Give the extent of all Plasmodium ovale-infected red blood cells.
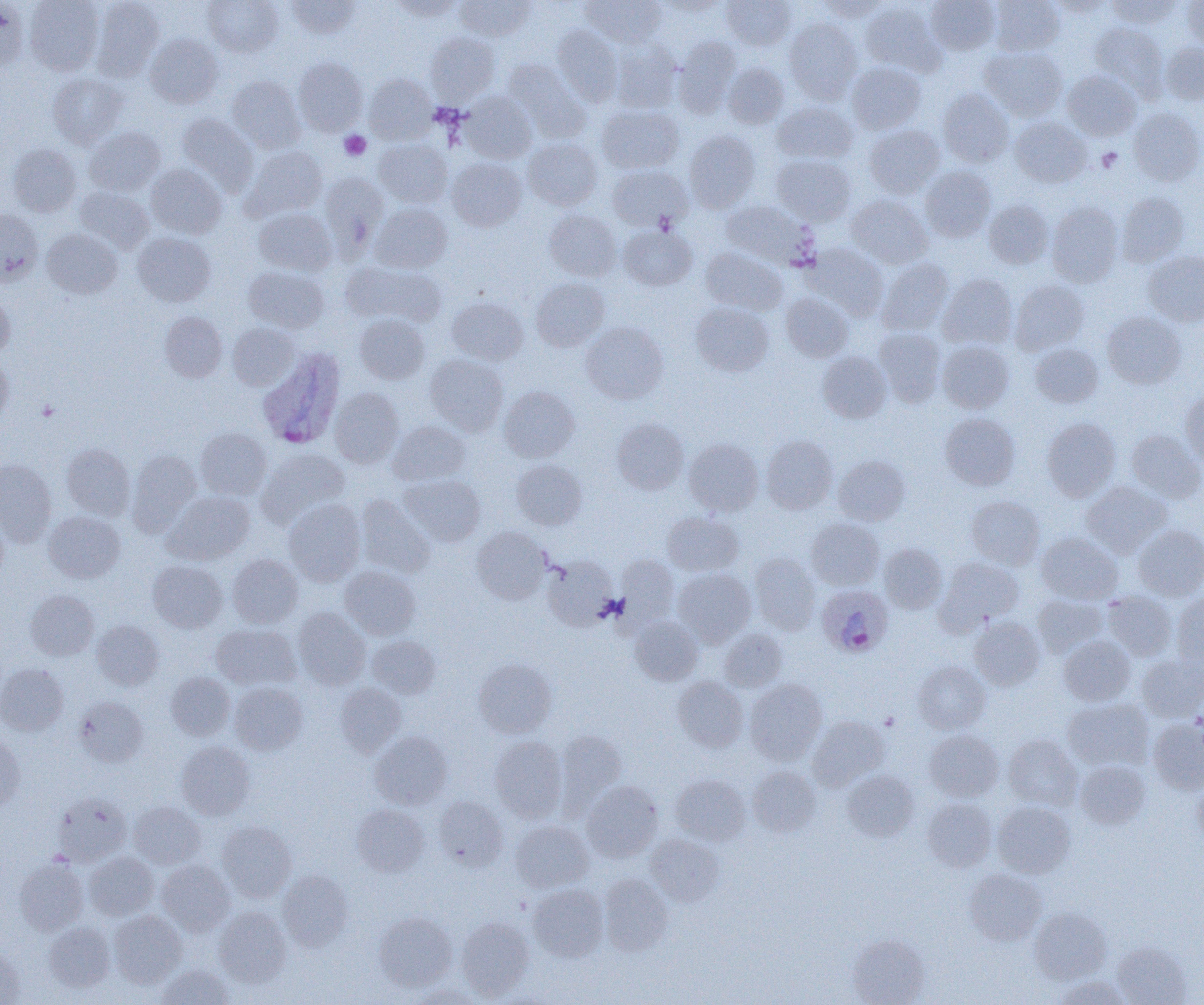

Approximate bounding boxes as named x1/y1/x2/y2 corners in pixels.
Plasmodium ovale-infected red blood cells: (x1=257, y1=348, x2=345, y2=449), (x1=816, y1=584, x2=893, y2=658).

Platelet locations: (x1=339, y1=131, x2=371, y2=160), (x1=1097, y1=148, x2=1122, y2=172), (x1=37, y1=400, x2=59, y2=421). Uninfected red blood cell locations: (x1=0, y1=0, x2=29, y2=74), (x1=24, y1=0, x2=104, y2=75), (x1=91, y1=0, x2=165, y2=81), (x1=203, y1=0, x2=283, y2=57), (x1=287, y1=0, x2=360, y2=39), (x1=389, y1=0, x2=464, y2=21), (x1=455, y1=0, x2=534, y2=41), (x1=582, y1=0, x2=665, y2=48), (x1=721, y1=0, x2=796, y2=50), (x1=813, y1=0, x2=890, y2=22), (x1=926, y1=0, x2=999, y2=55), (x1=989, y1=0, x2=1064, y2=56), (x1=1050, y1=0, x2=1112, y2=17), (x1=1106, y1=0, x2=1180, y2=28), (x1=1182, y1=0, x2=1204, y2=50), (x1=860, y1=2, x2=944, y2=77), (x1=784, y1=18, x2=862, y2=104), (x1=1091, y1=22, x2=1168, y2=97), (x1=552, y1=26, x2=622, y2=106), (x1=425, y1=32, x2=499, y2=105), (x1=145, y1=33, x2=223, y2=108), (x1=673, y1=36, x2=741, y2=116), (x1=610, y1=41, x2=682, y2=112), (x1=1160, y1=41, x2=1204, y2=105), (x1=980, y1=47, x2=1067, y2=121), (x1=292, y1=57, x2=368, y2=136), (x1=503, y1=60, x2=590, y2=142), (x1=723, y1=62, x2=789, y2=128), (x1=846, y1=62, x2=926, y2=134), (x1=1062, y1=70, x2=1141, y2=141), (x1=48, y1=73, x2=127, y2=148), (x1=364, y1=74, x2=436, y2=143), (x1=227, y1=76, x2=305, y2=152), (x1=938, y1=89, x2=1013, y2=167), (x1=459, y1=92, x2=536, y2=163), (x1=772, y1=101, x2=857, y2=164), (x1=597, y1=105, x2=683, y2=173), (x1=1128, y1=106, x2=1204, y2=186), (x1=177, y1=114, x2=258, y2=193), (x1=1010, y1=117, x2=1091, y2=187), (x1=863, y1=125, x2=944, y2=198), (x1=84, y1=127, x2=165, y2=196), (x1=684, y1=130, x2=760, y2=213), (x1=374, y1=138, x2=452, y2=207), (x1=523, y1=138, x2=602, y2=211), (x1=8, y1=143, x2=81, y2=216), (x1=242, y1=146, x2=327, y2=221), (x1=772, y1=154, x2=857, y2=226), (x1=447, y1=157, x2=527, y2=231), (x1=147, y1=164, x2=227, y2=239), (x1=608, y1=165, x2=692, y2=232), (x1=920, y1=165, x2=996, y2=242), (x1=320, y1=172, x2=388, y2=251), (x1=74, y1=186, x2=153, y2=253), (x1=1116, y1=191, x2=1190, y2=266), (x1=846, y1=194, x2=933, y2=268), (x1=720, y1=200, x2=818, y2=269), (x1=983, y1=200, x2=1053, y2=268), (x1=1047, y1=201, x2=1123, y2=287), (x1=371, y1=203, x2=451, y2=273), (x1=254, y1=208, x2=336, y2=276), (x1=0, y1=209, x2=42, y2=285), (x1=544, y1=209, x2=621, y2=282), (x1=619, y1=225, x2=698, y2=291), (x1=42, y1=228, x2=122, y2=298), (x1=132, y1=232, x2=215, y2=306), (x1=803, y1=242, x2=888, y2=320), (x1=700, y1=246, x2=787, y2=315), (x1=1143, y1=251, x2=1204, y2=326), (x1=877, y1=258, x2=954, y2=335), (x1=342, y1=261, x2=446, y2=327), (x1=243, y1=266, x2=329, y2=333), (x1=938, y1=274, x2=1018, y2=350), (x1=531, y1=278, x2=609, y2=351), (x1=1010, y1=280, x2=1089, y2=356), (x1=0, y1=289, x2=14, y2=357), (x1=781, y1=292, x2=853, y2=362), (x1=447, y1=296, x2=528, y2=365), (x1=690, y1=302, x2=773, y2=376), (x1=159, y1=311, x2=227, y2=382), (x1=1102, y1=311, x2=1185, y2=388), (x1=354, y1=314, x2=429, y2=384), (x1=581, y1=322, x2=668, y2=403), (x1=227, y1=323, x2=300, y2=389), (x1=874, y1=328, x2=946, y2=406), (x1=937, y1=340, x2=1014, y2=413), (x1=1030, y1=343, x2=1104, y2=408), (x1=816, y1=351, x2=891, y2=423), (x1=0, y1=353, x2=13, y2=423), (x1=425, y1=354, x2=508, y2=435), (x1=499, y1=386, x2=580, y2=462), (x1=330, y1=388, x2=404, y2=467), (x1=1181, y1=388, x2=1204, y2=469), (x1=940, y1=413, x2=1020, y2=490), (x1=1042, y1=417, x2=1121, y2=501), (x1=612, y1=418, x2=689, y2=494), (x1=388, y1=420, x2=470, y2=485), (x1=196, y1=428, x2=271, y2=499), (x1=1127, y1=429, x2=1204, y2=502), (x1=761, y1=436, x2=838, y2=514), (x1=684, y1=438, x2=764, y2=516), (x1=62, y1=443, x2=134, y2=520), (x1=128, y1=448, x2=201, y2=532), (x1=258, y1=448, x2=350, y2=527), (x1=833, y1=455, x2=910, y2=525), (x1=0, y1=459, x2=56, y2=544), (x1=512, y1=459, x2=588, y2=530), (x1=399, y1=475, x2=485, y2=546), (x1=1081, y1=481, x2=1172, y2=558), (x1=164, y1=491, x2=255, y2=564), (x1=355, y1=495, x2=435, y2=578), (x1=967, y1=496, x2=1045, y2=569), (x1=283, y1=499, x2=365, y2=586), (x1=0, y1=507, x2=8, y2=584), (x1=662, y1=511, x2=744, y2=576), (x1=44, y1=512, x2=124, y2=582), (x1=806, y1=518, x2=884, y2=590), (x1=1133, y1=524, x2=1204, y2=601), (x1=472, y1=527, x2=551, y2=604), (x1=1037, y1=532, x2=1122, y2=604), (x1=879, y1=543, x2=947, y2=613), (x1=749, y1=553, x2=820, y2=635), (x1=228, y1=554, x2=302, y2=628), (x1=542, y1=555, x2=617, y2=629), (x1=615, y1=555, x2=678, y2=628), (x1=936, y1=557, x2=1024, y2=631), (x1=148, y1=560, x2=228, y2=632), (x1=339, y1=566, x2=421, y2=639), (x1=673, y1=568, x2=755, y2=647), (x1=25, y1=590, x2=99, y2=660), (x1=1102, y1=591, x2=1177, y2=660), (x1=1172, y1=593, x2=1204, y2=673), (x1=1033, y1=594, x2=1107, y2=658), (x1=293, y1=608, x2=371, y2=689), (x1=630, y1=616, x2=703, y2=685), (x1=969, y1=616, x2=1045, y2=691), (x1=92, y1=619, x2=164, y2=690), (x1=211, y1=624, x2=300, y2=690), (x1=720, y1=628, x2=787, y2=692), (x1=366, y1=635, x2=441, y2=698), (x1=1058, y1=636, x2=1136, y2=706), (x1=1137, y1=654, x2=1204, y2=721), (x1=474, y1=658, x2=557, y2=738), (x1=912, y1=661, x2=990, y2=734), (x1=0, y1=663, x2=68, y2=736), (x1=166, y1=672, x2=235, y2=740), (x1=673, y1=676, x2=748, y2=752), (x1=745, y1=679, x2=827, y2=765), (x1=229, y1=682, x2=307, y2=755), (x1=334, y1=683, x2=406, y2=756), (x1=74, y1=696, x2=149, y2=767), (x1=1062, y1=698, x2=1153, y2=772), (x1=807, y1=715, x2=890, y2=791), (x1=1148, y1=718, x2=1204, y2=794), (x1=554, y1=729, x2=627, y2=813), (x1=925, y1=729, x2=1004, y2=801), (x1=370, y1=731, x2=452, y2=809), (x1=0, y1=732, x2=25, y2=811), (x1=1003, y1=734, x2=1082, y2=810), (x1=491, y1=736, x2=567, y2=822), (x1=176, y1=741, x2=255, y2=820), (x1=1075, y1=760, x2=1150, y2=829), (x1=748, y1=766, x2=821, y2=837), (x1=842, y1=770, x2=919, y2=841), (x1=670, y1=774, x2=750, y2=845), (x1=1192, y1=777, x2=1204, y2=851), (x1=582, y1=781, x2=663, y2=862), (x1=52, y1=792, x2=132, y2=866), (x1=433, y1=796, x2=507, y2=871), (x1=923, y1=798, x2=997, y2=872), (x1=129, y1=801, x2=205, y2=869), (x1=992, y1=801, x2=1075, y2=877), (x1=352, y1=804, x2=428, y2=877), (x1=216, y1=820, x2=296, y2=902), (x1=510, y1=820, x2=593, y2=892), (x1=646, y1=834, x2=724, y2=906), (x1=84, y1=852, x2=158, y2=920), (x1=14, y1=856, x2=88, y2=935), (x1=156, y1=860, x2=235, y2=936), (x1=964, y1=869, x2=1046, y2=946), (x1=277, y1=870, x2=353, y2=951), (x1=599, y1=874, x2=673, y2=956), (x1=529, y1=884, x2=608, y2=961), (x1=214, y1=906, x2=292, y2=987), (x1=1030, y1=907, x2=1112, y2=984), (x1=108, y1=910, x2=187, y2=989), (x1=374, y1=911, x2=457, y2=990), (x1=456, y1=917, x2=534, y2=1000), (x1=44, y1=922, x2=115, y2=993), (x1=848, y1=933, x2=930, y2=1005), (x1=1111, y1=942, x2=1192, y2=1005), (x1=0, y1=946, x2=25, y2=1004), (x1=156, y1=964, x2=233, y2=1005), (x1=1053, y1=976, x2=1132, y2=1005), (x1=408, y1=985, x2=485, y2=1005). Slide-level diagnosis: Plasmodium ovale. 1000x magnification. One field of a larger specimen. Image is 1204×1005 pixels. Light microscopy. Thin blood smear.